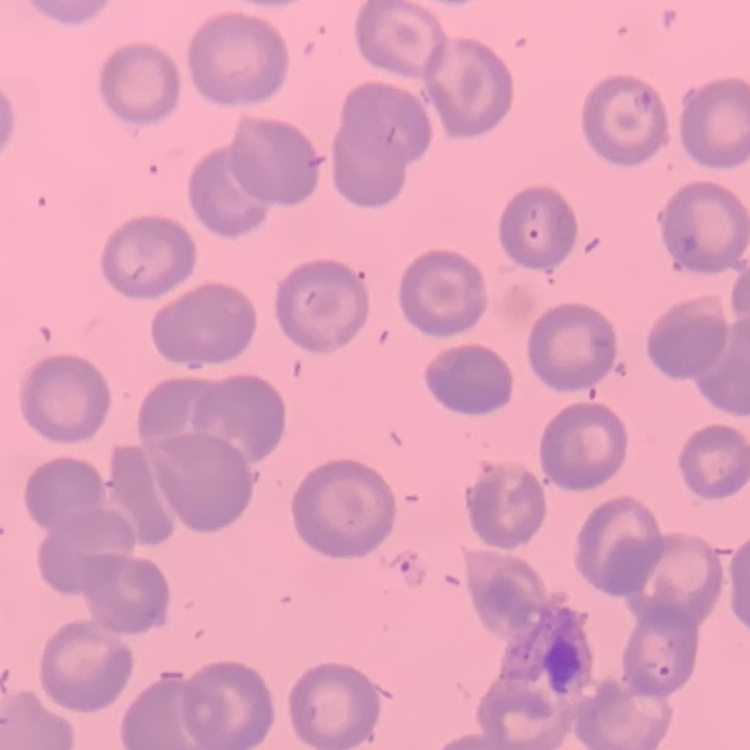 The red blood cells exhibit no rouleaux formation. One tile cut from a larger photomicrograph. Thin blood film. Stained with either Field's or Giemsa.